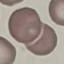

Summary:
  - Result: no malaria parasites seen
  - Stain: Giemsa
  - Preparation: thin smear
  - Capture: smartphone through the microscope eyepiece
  - Image type: automatically extracted cell patch, resized to 64 × 64 pixels